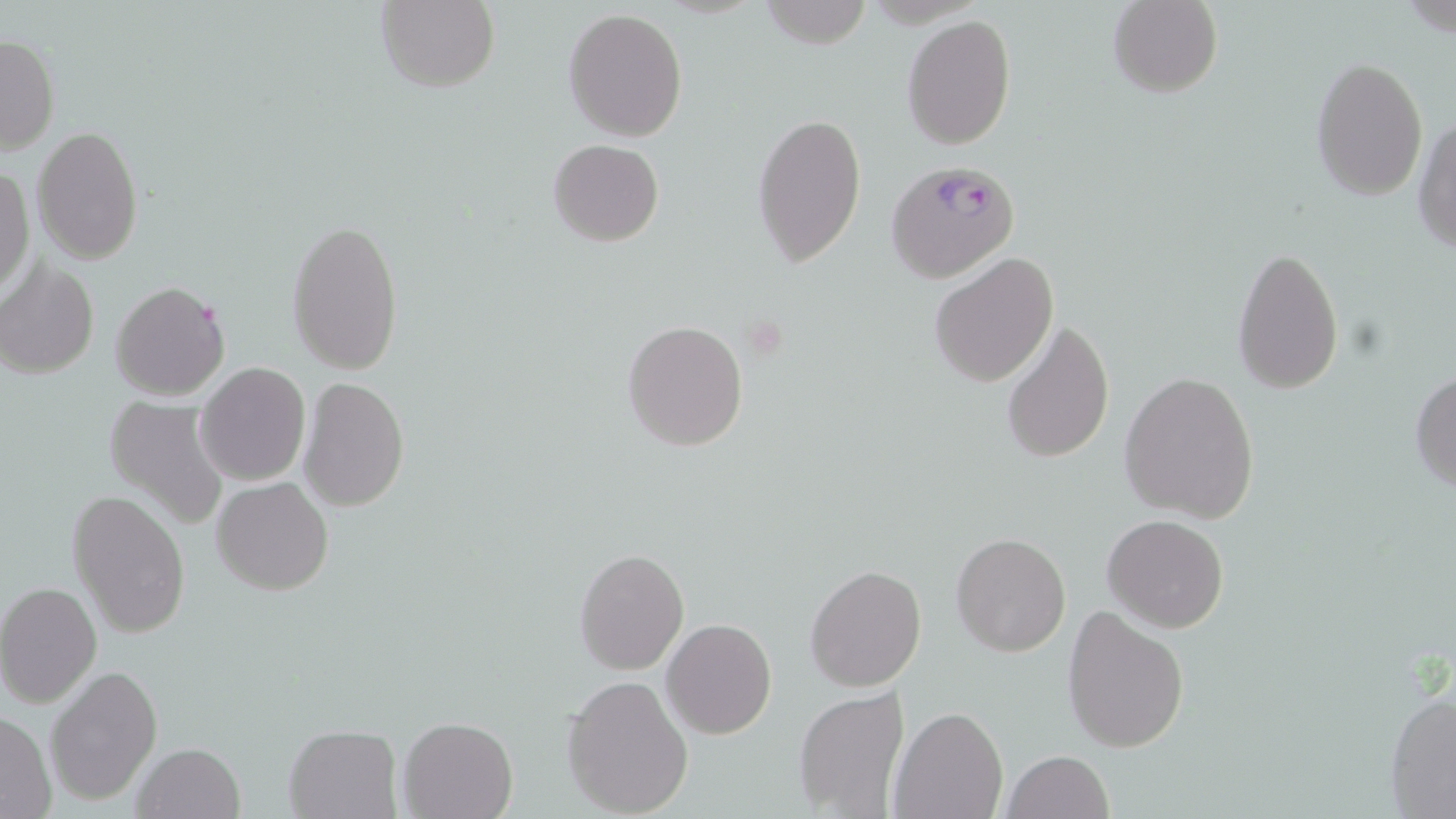 Approximate bounding boxes as (x1,y1)-(x2,y2) corner pairs in pixels. Uninfected red blood cell locations: (376,0)-(500,94), (761,0)-(871,49), (1108,0)-(1222,98), (563,7)-(688,141), (900,15)-(1016,151), (1,33)-(59,156), (1311,56)-(1429,201), (752,108)-(867,269), (1412,115)-(1456,256), (32,126)-(143,263), (548,139)-(663,247), (0,167)-(33,300), (286,216)-(404,376), (1229,246)-(1345,395), (929,253)-(1058,389), (1,261)-(102,378), (110,280)-(230,400), (1000,316)-(1116,466), (622,318)-(750,453), (196,365)-(311,486), (1408,369)-(1456,493), (1119,371)-(1260,524), (299,379)-(408,513), (103,397)-(233,528), (213,476)-(334,597), (67,489)-(190,637), (1103,515)-(1228,632), (952,533)-(1071,657), (573,547)-(688,674), (805,563)-(927,691), (1,582)-(100,707), (1061,605)-(1190,755), (662,618)-(777,738), (46,664)-(161,805), (561,676)-(693,817), (1384,686)-(1456,818), (793,687)-(910,817), (890,706)-(1006,819), (0,709)-(56,817), (398,717)-(519,819), (283,726)-(401,818), (131,742)-(246,819), (1002,750)-(1114,819). Plasmodium falciparum-infected red blood cell locations: (886,158)-(1020,284). Slide-level diagnosis: Plasmodium falciparum. Light microscopy. May-Grünwald-Giemsa stain. Image is 1456×819 pixels. 1000x magnification. One field of a larger specimen. Thin blood film.